Report the malaria status of this cell.
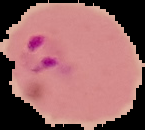
It is parasitized.

{
  "image_size": "145×130 pixels",
  "image_type": "segmented cell region with the area outside set to black",
  "preparation": "thin blood film"
}